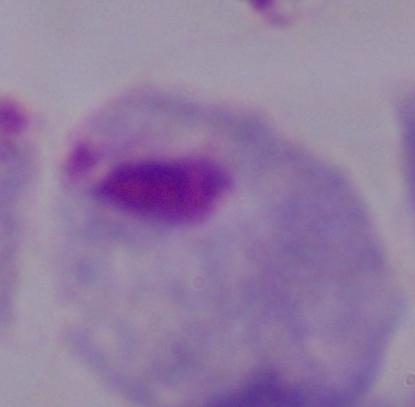 Photomicrograph. 1000x magnification. A trichomonad is shown.